Locate every blood parasite and identify its species.
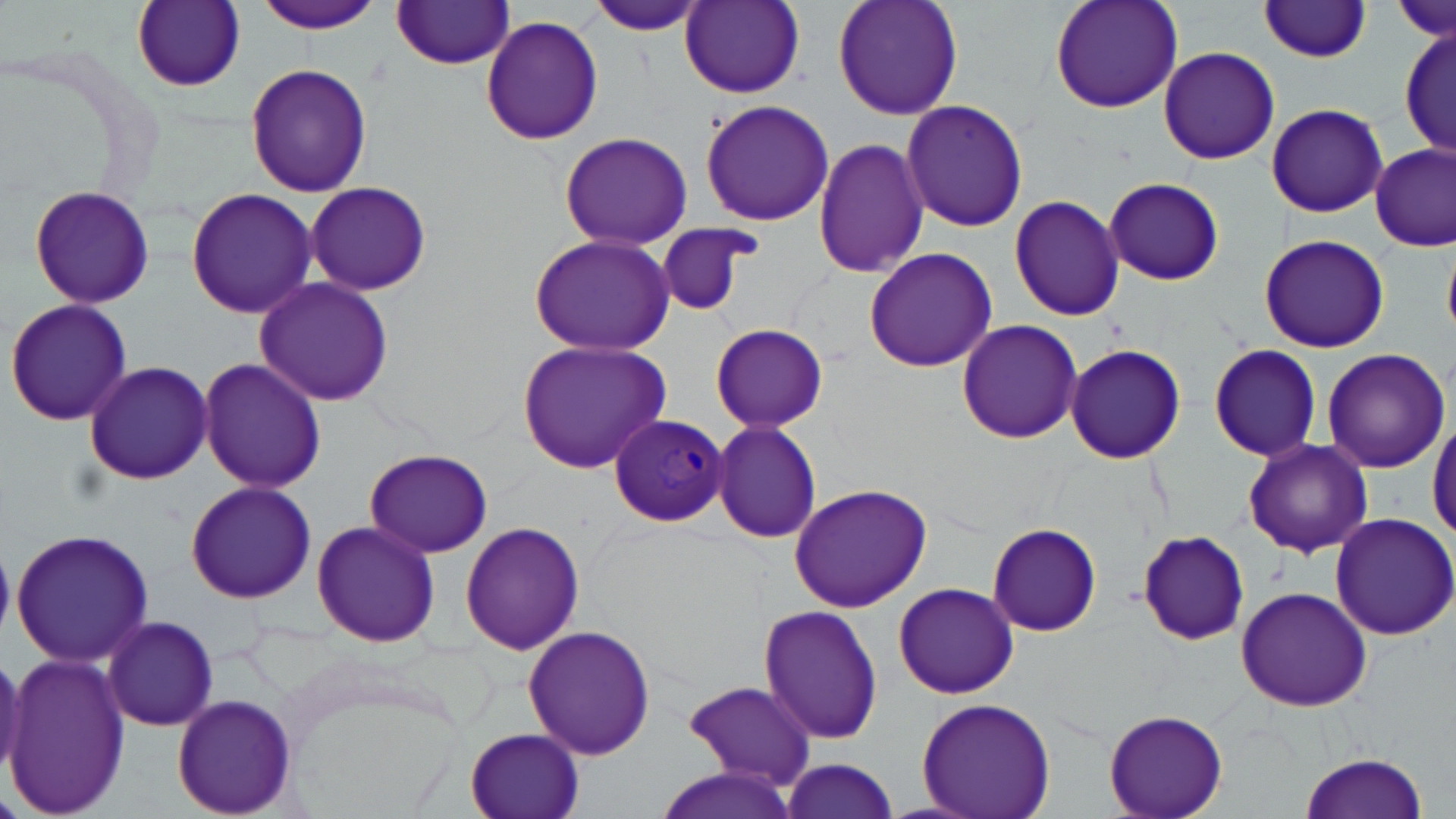
Approximate bounding boxes as [x1, y1, x2, y2] in pixels.
Plasmodium malariae-infected red blood cells: [609, 411, 730, 527].
No Plasmodium falciparum, Plasmodium ovale, Plasmodium vivax, Babesia divergens, or Trypanosoma brucei observed.

slide-level diagnosis = Plasmodium malariae
stain = May-Grünwald-Giemsa
modality = light microscopy
magnification = 1000x
field of view = one of a larger specimen
image size = 1456×819 pixels
preparation = thin blood smear
uninfected red blood cell locations = approximate bounding boxes as [x1, y1, x2, y2] in pixels: [251, 0, 387, 34], [680, 0, 805, 97], [831, 0, 965, 120], [1049, 0, 1184, 113], [1395, 0, 1453, 47], [130, 1, 245, 91], [390, 1, 517, 69], [1257, 2, 1375, 62], [588, 3, 706, 38], [480, 15, 604, 145], [1398, 23, 1453, 161], [1159, 46, 1280, 165], [244, 61, 372, 198], [700, 98, 836, 227], [901, 98, 1029, 232], [1265, 102, 1388, 217], [559, 131, 694, 250], [813, 135, 929, 279], [1372, 145, 1454, 251], [1103, 178, 1226, 284], [304, 180, 433, 297], [28, 185, 155, 310], [185, 187, 319, 319], [1008, 193, 1126, 321], [653, 222, 758, 318], [1258, 231, 1390, 354], [1443, 233, 1456, 340], [529, 234, 674, 355], [863, 247, 999, 374], [253, 275, 395, 407], [3, 298, 133, 429], [956, 319, 1082, 444], [709, 322, 830, 433], [516, 338, 672, 472], [1207, 342, 1322, 462], [1065, 344, 1186, 464], [1322, 348, 1450, 473], [196, 357, 329, 493], [84, 360, 214, 486], [1429, 412, 1456, 544], [712, 421, 825, 543], [1241, 437, 1374, 558], [362, 448, 495, 559], [183, 480, 318, 605], [788, 483, 932, 612], [1328, 513, 1456, 643], [310, 520, 441, 648], [459, 520, 585, 654], [987, 521, 1102, 637], [10, 527, 155, 670], [1137, 531, 1247, 646], [891, 580, 1020, 700], [1234, 585, 1373, 712], [758, 604, 884, 744], [101, 614, 220, 733], [522, 625, 658, 760], [2, 653, 132, 817], [680, 681, 818, 791], [171, 694, 298, 818], [914, 697, 1057, 819], [1103, 709, 1227, 819], [465, 728, 586, 819], [1295, 750, 1431, 819], [780, 757, 901, 819], [647, 763, 804, 819]